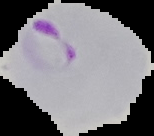

Summary:
  - Preparation: thin blood smear
  - Image type: cell region segmented out of the field of view; surrounding area masked to black
  - Malaria status: parasitized
  - Image size: 154×136 pixels